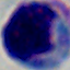

Summary:
  - Magnification: 1000x
  - Identification: white blood cell
  - Modality: photomicrograph